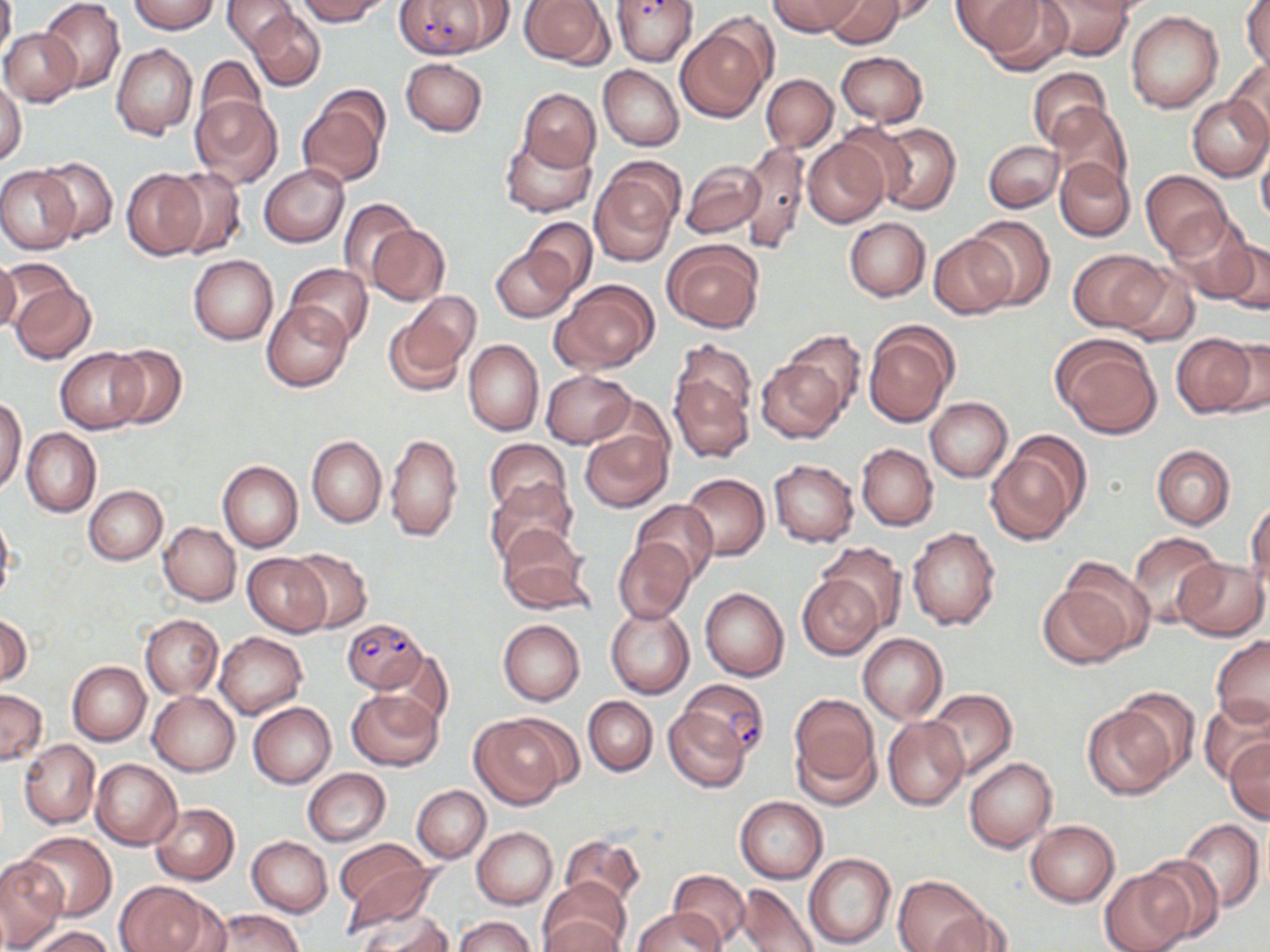

slide-level diagnosis = Plasmodium falciparum
uninfected red blood cell locations = approximate bounding boxes as (x1, y1, x2, y2) in pixels: (0, 0, 16, 65), (39, 0, 124, 93), (130, 0, 219, 34), (223, 0, 298, 52), (297, 0, 389, 25), (518, 0, 613, 68), (767, 0, 861, 36), (824, 0, 905, 47), (860, 0, 941, 23), (950, 0, 1043, 54), (979, 0, 1074, 74), (1242, 0, 1269, 76), (1036, 1, 1138, 60), (1125, 11, 1223, 113), (249, 12, 324, 91), (674, 22, 771, 123), (1, 27, 81, 107), (112, 44, 198, 140), (835, 51, 929, 126), (195, 56, 268, 135), (400, 58, 488, 136), (1226, 58, 1270, 142), (599, 65, 683, 151), (1026, 68, 1112, 149), (761, 74, 837, 152), (0, 77, 26, 167), (297, 89, 388, 188), (519, 89, 599, 172), (1187, 95, 1270, 181), (191, 96, 281, 188), (1047, 102, 1132, 196), (872, 122, 961, 216), (501, 133, 595, 217), (802, 136, 890, 228), (738, 140, 811, 255), (984, 141, 1062, 213), (1256, 144, 1270, 230), (34, 156, 118, 243), (1052, 158, 1134, 242), (682, 161, 764, 238), (590, 163, 680, 263), (259, 165, 349, 247), (163, 166, 247, 259), (0, 167, 78, 254), (122, 168, 205, 258), (1140, 170, 1231, 259), (338, 198, 418, 284), (966, 215, 1054, 308), (1169, 215, 1255, 304), (524, 217, 597, 297), (845, 217, 929, 301), (367, 223, 449, 306), (928, 235, 1017, 318), (1217, 238, 1270, 316), (662, 240, 763, 332), (490, 245, 578, 322), (1070, 249, 1163, 332), (188, 254, 278, 345), (0, 257, 20, 333), (3, 258, 78, 324), (1111, 263, 1199, 345), (285, 264, 372, 345), (551, 279, 659, 374), (9, 281, 96, 363), (386, 294, 481, 395), (263, 301, 353, 391), (863, 321, 959, 429), (780, 331, 865, 419), (1051, 333, 1162, 439), (1171, 335, 1257, 418), (1216, 336, 1270, 417), (463, 338, 543, 436), (105, 344, 187, 429), (56, 347, 145, 433), (757, 361, 844, 443), (669, 369, 754, 464), (542, 370, 637, 448), (925, 397, 1013, 482), (1, 398, 27, 495), (22, 428, 100, 517), (579, 428, 672, 513), (384, 432, 464, 542), (985, 434, 1087, 543), (306, 435, 386, 527), (485, 438, 571, 518), (857, 443, 937, 531), (1152, 445, 1235, 529), (218, 460, 302, 553), (769, 460, 858, 547), (681, 473, 769, 561), (486, 480, 577, 564), (84, 485, 167, 565), (1247, 499, 1269, 593), (632, 500, 719, 584), (0, 509, 15, 605), (158, 522, 240, 605), (497, 525, 592, 613), (908, 527, 1001, 630), (1127, 532, 1225, 628), (613, 537, 695, 624), (816, 541, 907, 632), (288, 548, 372, 633), (243, 554, 331, 636), (1058, 558, 1155, 654), (1173, 558, 1267, 640), (796, 574, 883, 659), (1039, 583, 1132, 668), (699, 587, 789, 681), (606, 607, 693, 698), (0, 612, 31, 686), (140, 614, 222, 698), (499, 620, 585, 706), (214, 631, 306, 719), (858, 632, 948, 724), (1211, 636, 1269, 728), (379, 648, 453, 729), (68, 660, 150, 746), (1, 688, 46, 764), (347, 688, 442, 771), (925, 688, 1016, 780), (1117, 688, 1201, 781), (148, 691, 239, 776), (788, 693, 879, 794), (582, 696, 658, 775), (1199, 698, 1270, 787), (248, 702, 335, 788), (1082, 702, 1180, 798), (663, 706, 750, 793), (470, 715, 570, 808), (883, 716, 968, 810), (20, 739, 99, 828), (1225, 740, 1270, 824), (964, 756, 1057, 853), (90, 758, 181, 849), (303, 768, 390, 846), (412, 784, 490, 862), (735, 796, 827, 883), (151, 803, 238, 885), (1176, 819, 1264, 913), (1025, 820, 1120, 906), (472, 827, 558, 908), (21, 831, 117, 919), (560, 834, 645, 913), (247, 836, 331, 917), (338, 850, 439, 935), (804, 852, 896, 949), (1137, 854, 1225, 942), (0, 856, 66, 949), (669, 869, 751, 948), (1100, 870, 1189, 952), (893, 875, 991, 951), (539, 877, 628, 952), (116, 881, 213, 952), (735, 883, 819, 952), (210, 908, 304, 951), (632, 908, 722, 952), (933, 908, 1016, 952), (357, 911, 456, 952), (542, 915, 624, 952), (455, 916, 534, 952), (29, 926, 115, 952)
field of view = single
modality = light microscopy
Plasmodium falciparum-infected red blood cell locations = approximate bounding boxes as (x1, y1, x2, y2) in pixels: (395, 0, 500, 59), (611, 1, 697, 66), (343, 617, 426, 692), (676, 679, 769, 761)
stain = May-Grünwald-Giemsa
image size = 1270×952 pixels
preparation = thin blood film
magnification = 1000x